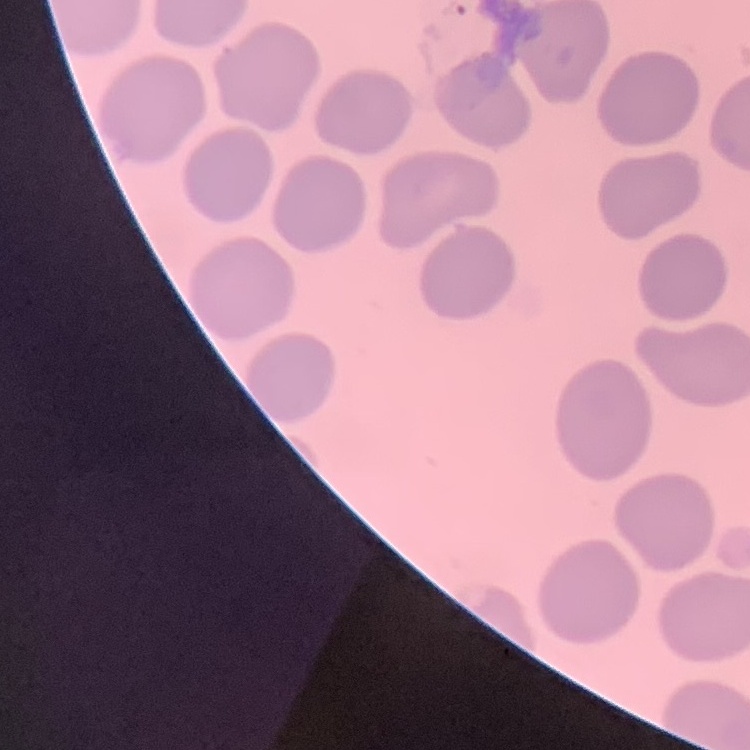
red blood cell morphology = no rouleaux formation
preparation = thin blood smear
stain = Field's or Giemsa
image type = square crop of a larger photomicrograph